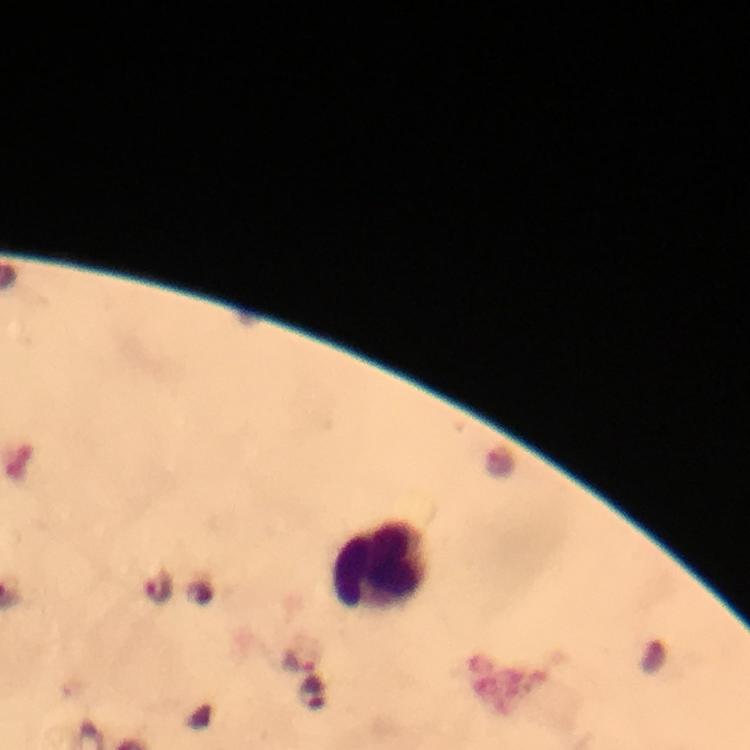

Approximate centers as {x, y} in pixels.
Summary:
  - Plasmodium parasite locations: {159, 587}, {316, 695}
  - Leukocyte locations: {380, 565}
  - Image size: 750×750 pixels
  - Context: from a diagnostic examination for malaria
  - Stain: Giemsa
  - Cropped from: one field of view
  - Magnification: 100x
  - Capture: smartphone photograph through a microscope
  - Preparation: thick blood smear
  - Immersion oil: used